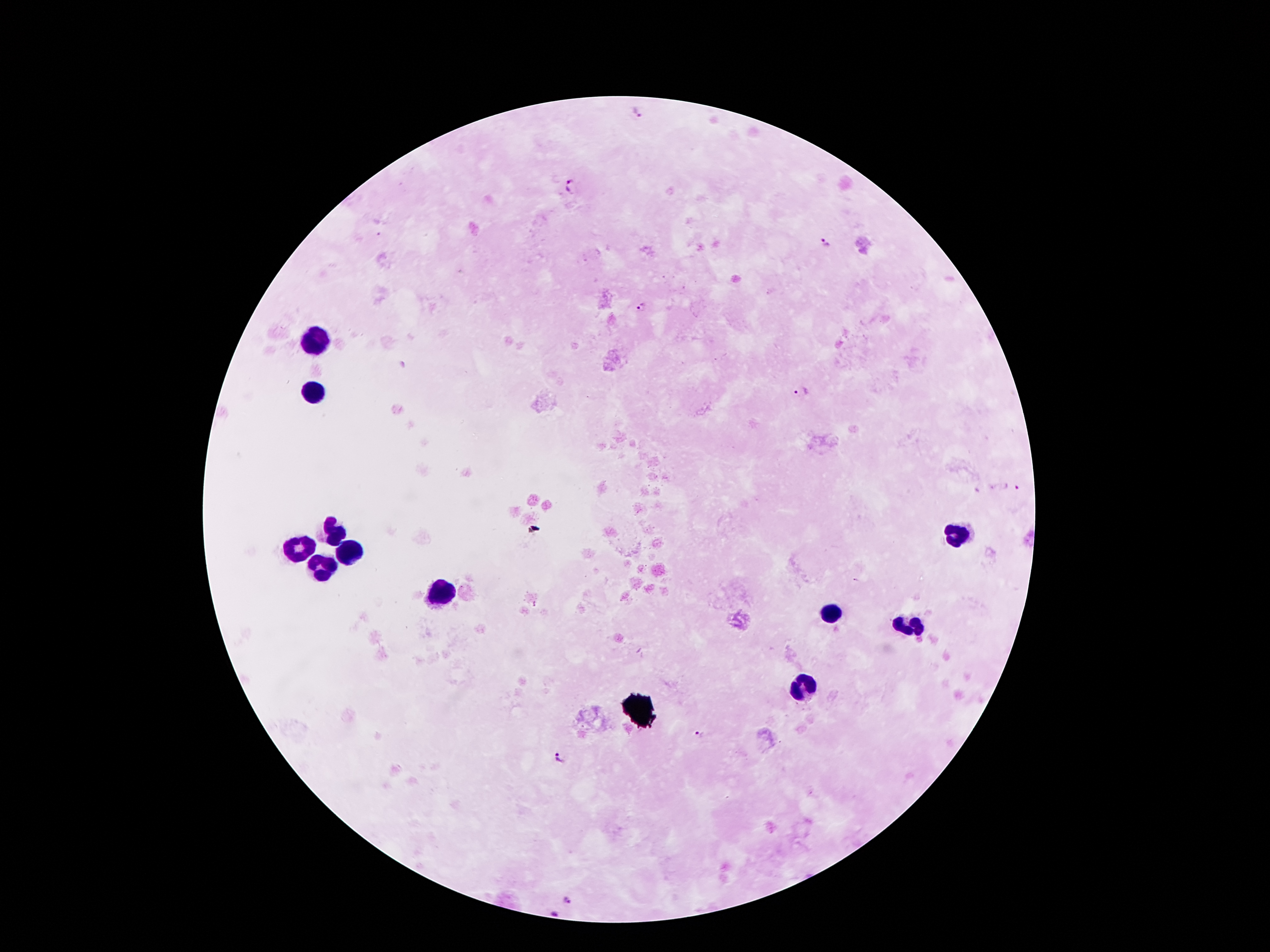
Approximate centers as {x, y} in pixels.
Summary:
  - Plasmodium parasite locations: {637, 112}, {570, 187}, {822, 242}, {642, 307}, {801, 391}, {1010, 488}, {699, 735}, {562, 758}, {567, 898}
  - Leukocyte locations: {314, 343}, {312, 394}, {332, 534}, {958, 541}, {345, 546}, {294, 549}, {322, 564}, {444, 595}, {831, 610}, {905, 625}, {808, 686}
  - Capture: smartphone camera through the microscope eyepiece
  - Stain: Giemsa
  - Image size: 1270×952 pixels
  - Field of view: single
  - Magnification: 100x
  - Preparation: thick blood smear
  - Patient malaria status: positive for Plasmodium falciparum